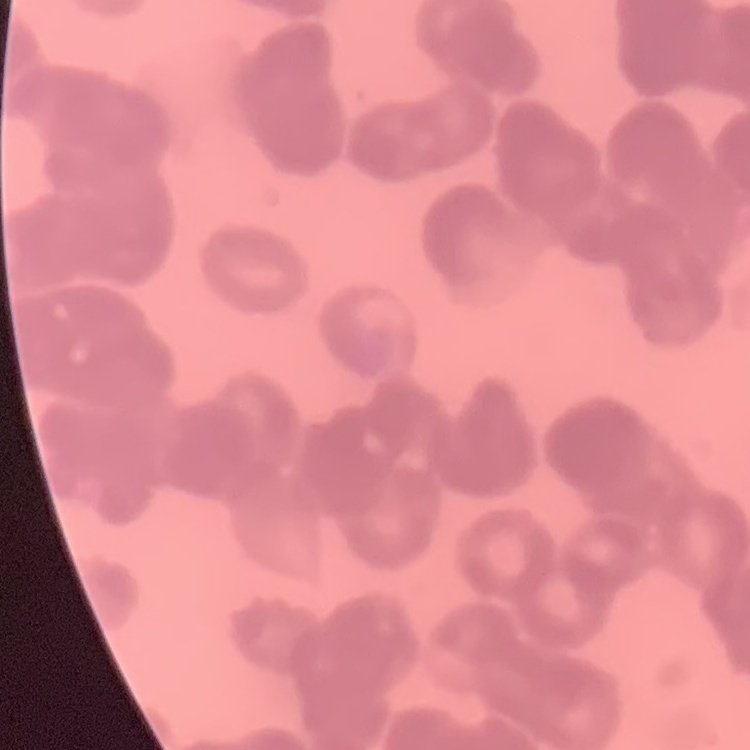 The red blood cells show rouleaux formation. Thin peripheral smear. Square crop of a larger photomicrograph. Stained with either Field's or Giemsa.